Assess the morphology of the red blood cells.
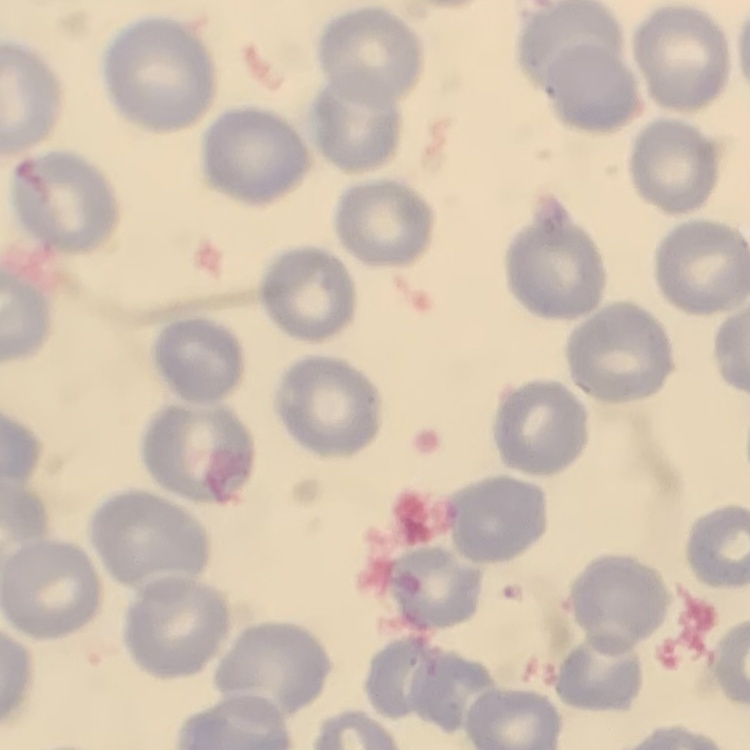

They show no rouleaux formation.

Summary:
  - Preparation: thin peripheral smear
  - Stain: Field's or Giemsa
  - Image type: one tile cut from a larger photomicrograph